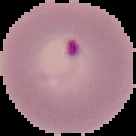 Result: Plasmodium parasites identified. Image is 136×136 pixels. From a thin blood film. Segmented cell region on a black background.